Report the malaria status of this cell.
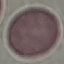

It is uninfected.

Automatically extracted cell patch, resized to 64 × 64 pixels. Giemsa-stained preparation. Photographed with a smartphone camera at the microscope eyepiece. Thin blood film.